Give the position of every leukocyte visible.
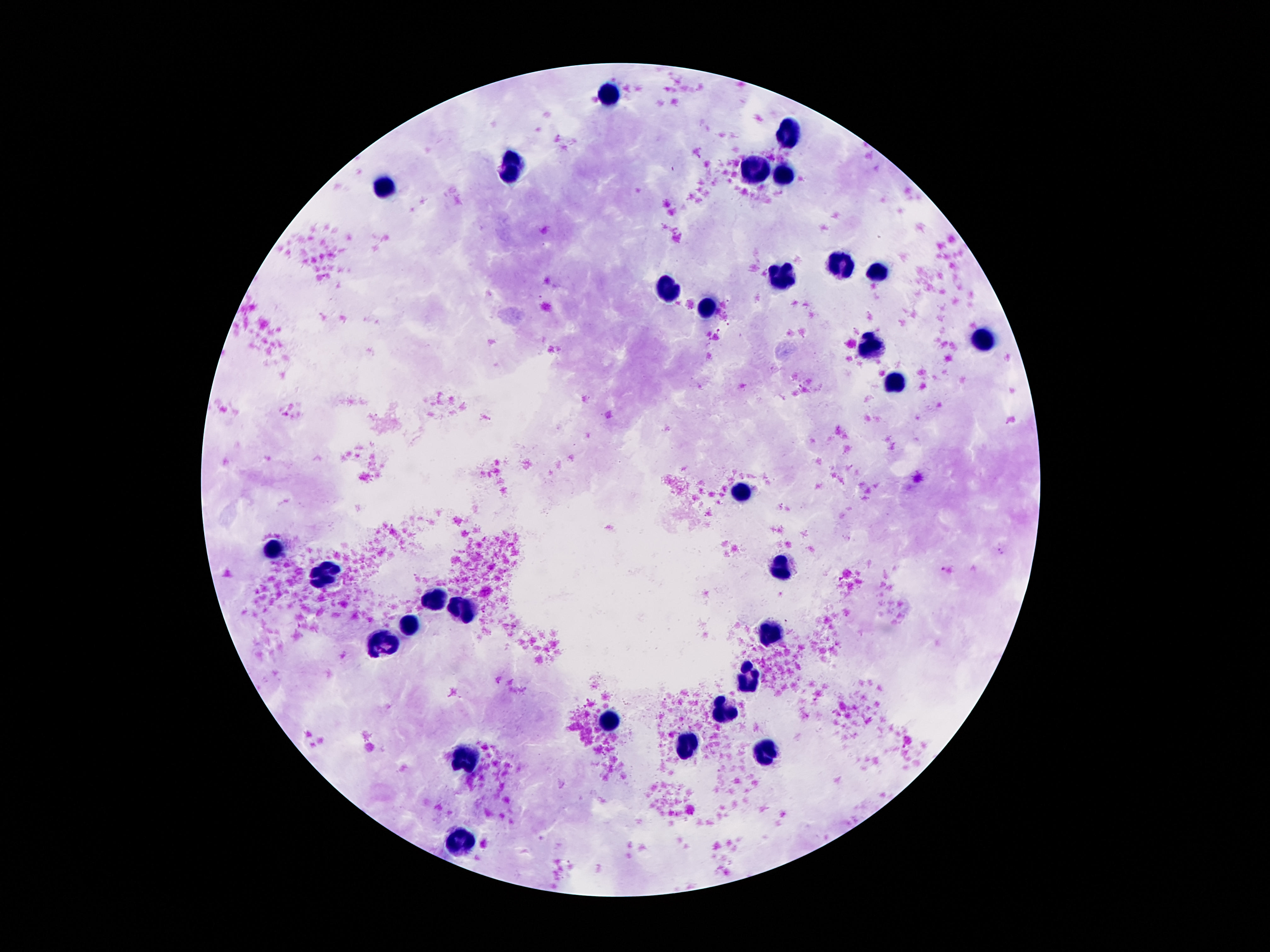
Approximate object centers, in pixels from the top-left corner.
Leukocytes: (x=607, y=93), (x=788, y=136), (x=515, y=167), (x=756, y=170), (x=788, y=176), (x=385, y=188), (x=840, y=264), (x=877, y=274), (x=782, y=279), (x=668, y=292), (x=709, y=307), (x=984, y=337), (x=868, y=345), (x=896, y=386), (x=741, y=489), (x=273, y=550), (x=782, y=569), (x=323, y=573), (x=433, y=598), (x=463, y=609), (x=411, y=624), (x=771, y=631), (x=385, y=641), (x=749, y=680), (x=724, y=710), (x=610, y=723), (x=689, y=747), (x=765, y=751), (x=469, y=757), (x=463, y=842).

patient_malaria_status: not infected
stain: Giemsa
magnification: 100x
capture: smartphone camera through the microscope eyepiece
image_size: 1270×952 pixels
preparation: thick blood smear
field_of_view: one from this slide